Report the malaria status of this cell.
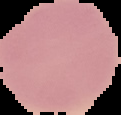
It is uninfected.

preparation = thin blood smear
image type = segmented cell region on a black background
image size = 121×115 pixels